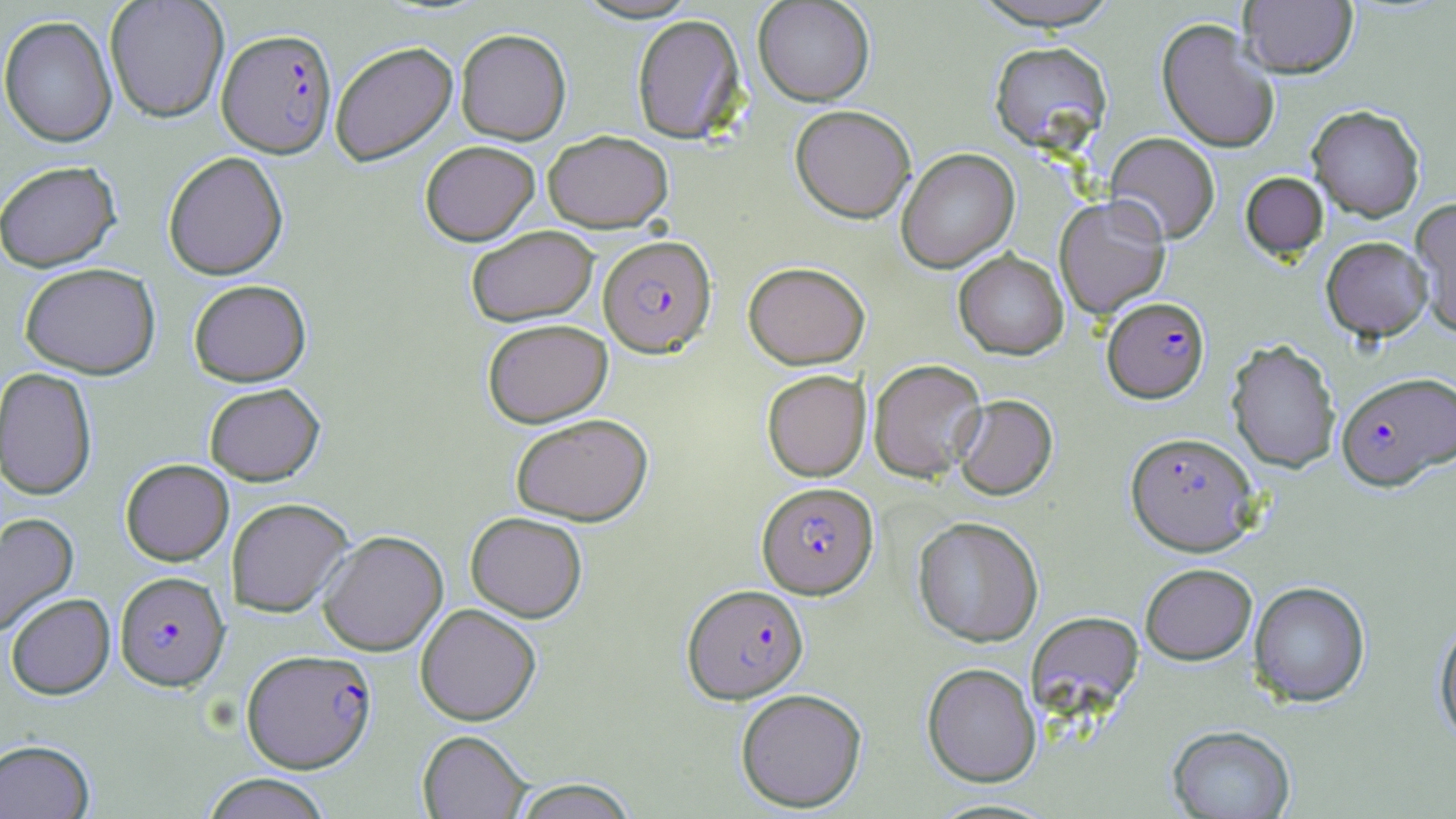
Approximate bounding boxes as named x1/y1/x2/y2 corners in pixels. Plasmodium falciparum-infected red blood cell locations: (x1=216, y1=27, x2=338, y2=158), (x1=598, y1=235, x2=716, y2=356), (x1=1103, y1=296, x2=1209, y2=402), (x1=1336, y1=370, x2=1456, y2=489), (x1=1124, y1=431, x2=1261, y2=555), (x1=757, y1=481, x2=877, y2=599), (x1=115, y1=570, x2=230, y2=690), (x1=682, y1=583, x2=808, y2=703), (x1=242, y1=648, x2=376, y2=773). Uninfected red blood cell locations: (x1=104, y1=0, x2=230, y2=123), (x1=971, y1=0, x2=1123, y2=30), (x1=1240, y1=0, x2=1358, y2=78), (x1=753, y1=1, x2=875, y2=106), (x1=632, y1=13, x2=746, y2=143), (x1=0, y1=14, x2=118, y2=147), (x1=1156, y1=18, x2=1280, y2=153), (x1=455, y1=28, x2=571, y2=145), (x1=329, y1=41, x2=458, y2=166), (x1=989, y1=41, x2=1112, y2=152), (x1=790, y1=104, x2=916, y2=222), (x1=1307, y1=104, x2=1425, y2=222), (x1=543, y1=129, x2=673, y2=232), (x1=1105, y1=132, x2=1220, y2=244), (x1=420, y1=140, x2=540, y2=245), (x1=896, y1=147, x2=1019, y2=273), (x1=162, y1=151, x2=289, y2=279), (x1=0, y1=160, x2=121, y2=272), (x1=1240, y1=172, x2=1328, y2=260), (x1=1054, y1=195, x2=1170, y2=319), (x1=1409, y1=198, x2=1456, y2=337), (x1=466, y1=225, x2=598, y2=327), (x1=1321, y1=236, x2=1432, y2=341), (x1=953, y1=249, x2=1068, y2=360), (x1=743, y1=261, x2=870, y2=369), (x1=19, y1=262, x2=161, y2=379), (x1=188, y1=279, x2=312, y2=386), (x1=482, y1=318, x2=612, y2=427), (x1=1226, y1=339, x2=1341, y2=473), (x1=868, y1=359, x2=987, y2=482), (x1=0, y1=367, x2=97, y2=500), (x1=762, y1=369, x2=870, y2=481), (x1=204, y1=383, x2=325, y2=485), (x1=953, y1=394, x2=1058, y2=500), (x1=510, y1=413, x2=653, y2=526), (x1=120, y1=459, x2=234, y2=565), (x1=226, y1=497, x2=353, y2=617), (x1=465, y1=511, x2=587, y2=622), (x1=0, y1=512, x2=79, y2=636), (x1=913, y1=516, x2=1043, y2=646), (x1=318, y1=529, x2=448, y2=656), (x1=1140, y1=562, x2=1256, y2=665), (x1=1248, y1=580, x2=1371, y2=707), (x1=5, y1=593, x2=115, y2=699), (x1=415, y1=603, x2=541, y2=726), (x1=1027, y1=611, x2=1144, y2=718), (x1=1433, y1=616, x2=1456, y2=747), (x1=921, y1=662, x2=1041, y2=787), (x1=734, y1=688, x2=867, y2=813), (x1=1166, y1=724, x2=1296, y2=818), (x1=417, y1=729, x2=532, y2=818), (x1=0, y1=739, x2=95, y2=819), (x1=200, y1=773, x2=334, y2=819), (x1=510, y1=778, x2=640, y2=818). Slide-level diagnosis: Plasmodium falciparum. May-Grünwald-Giemsa-stained preparation. Light microscopy. 1000x magnification. Thin blood film. Image is 1456×819 pixels. Single field of view.